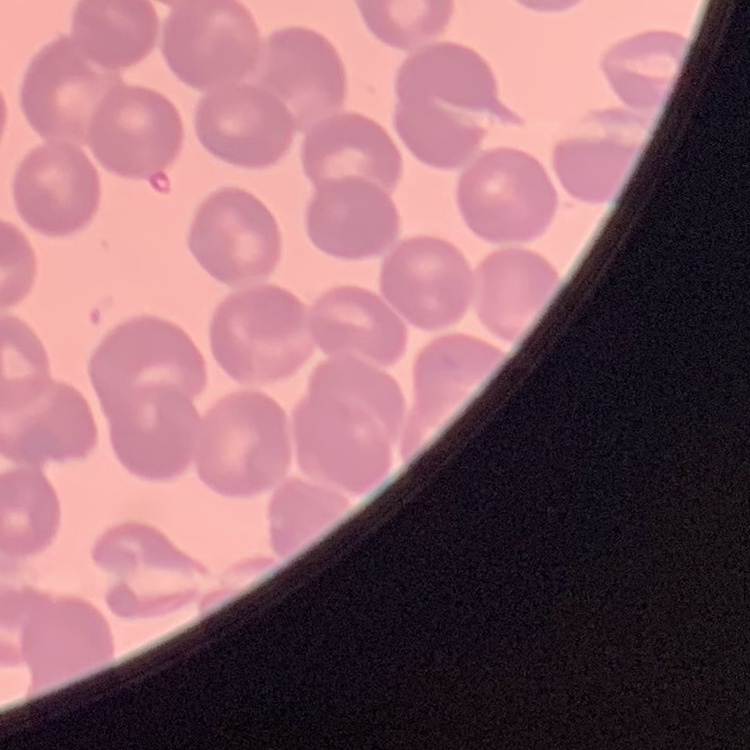
Summary:
  - Erythrocyte morphology: no rouleaux formation
  - Preparation: thin blood smear
  - Image type: square crop of a larger photomicrograph
  - Stain: Field's or Giemsa